Give the extent of all Plasmodium falciparum-infected red blood cells.
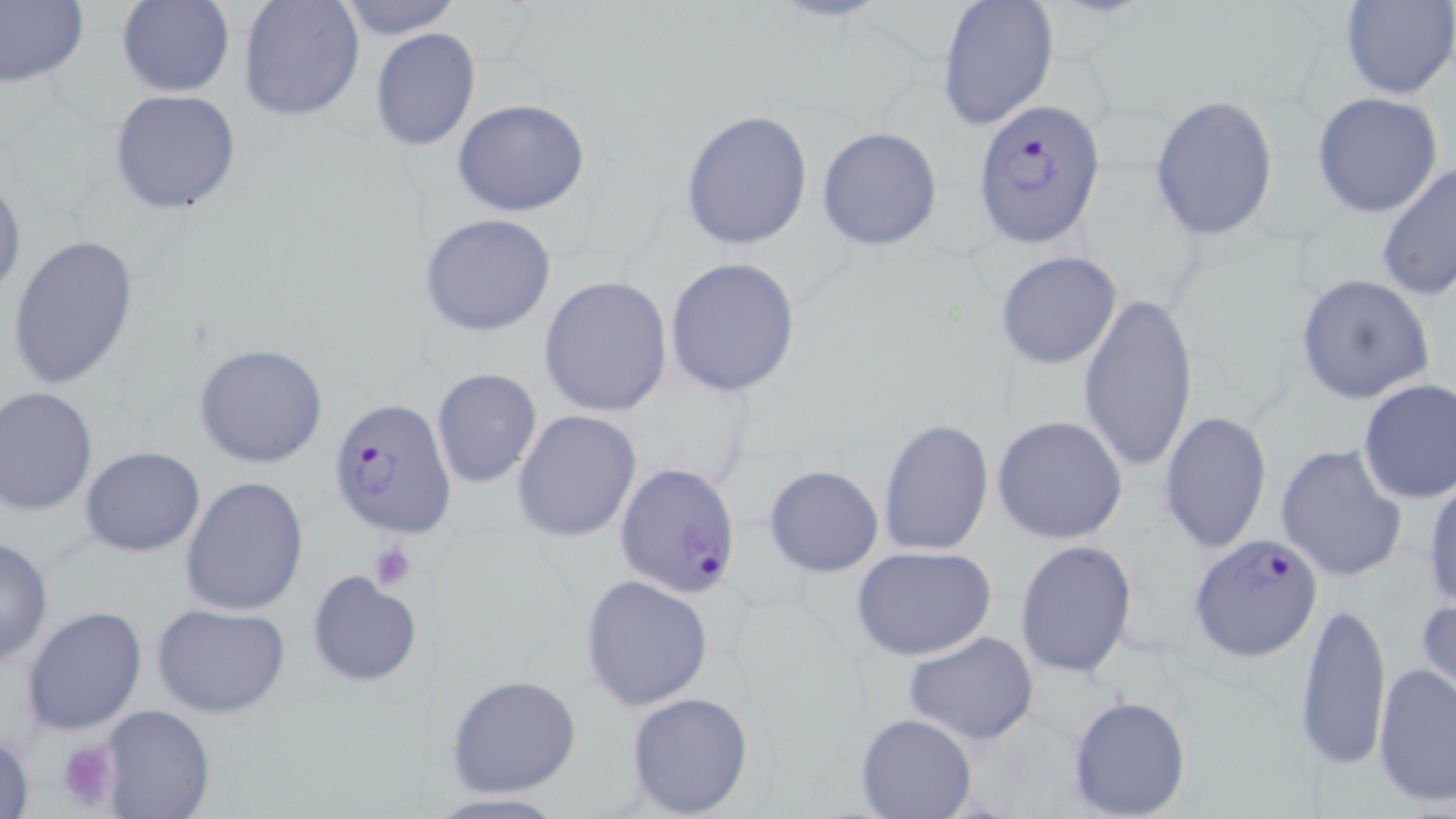

Approximate bounding boxes as (x1, y1, x2, y2) in pixels.
Plasmodium falciparum-infected red blood cells: (973, 98, 1106, 249), (327, 397, 459, 540), (615, 462, 744, 599), (1190, 535, 1324, 662).

Summary:
  - Platelet locations: (367, 544, 417, 590), (58, 739, 123, 813)
  - Uninfected red blood cell locations: (116, 0, 234, 98), (238, 0, 365, 121), (337, 0, 462, 38), (1339, 0, 1456, 101), (0, 1, 88, 87), (937, 1, 1059, 131), (369, 29, 481, 152), (109, 90, 241, 214), (1311, 91, 1444, 218), (1149, 94, 1279, 240), (451, 99, 592, 218), (681, 108, 814, 252), (817, 126, 944, 250), (1378, 163, 1455, 301), (0, 173, 24, 303), (421, 213, 558, 337), (7, 232, 140, 390), (996, 251, 1122, 370), (664, 258, 803, 398), (1295, 273, 1436, 404), (540, 275, 673, 417), (1079, 290, 1198, 476), (195, 344, 329, 467), (431, 368, 542, 490), (1356, 379, 1456, 504), (0, 386, 98, 516), (512, 410, 642, 544), (1159, 410, 1272, 554), (992, 414, 1128, 544), (878, 418, 994, 557), (1277, 444, 1408, 584), (79, 446, 206, 556), (764, 465, 884, 576), (181, 475, 310, 617), (1423, 476, 1456, 612), (0, 535, 54, 667), (1014, 540, 1139, 680), (852, 546, 996, 661), (306, 569, 423, 686), (579, 574, 714, 709), (1416, 594, 1456, 708), (1294, 600, 1392, 771), (152, 604, 291, 717), (20, 605, 149, 735), (902, 631, 1040, 745), (1374, 662, 1455, 810), (445, 674, 582, 798), (624, 691, 754, 818), (1066, 694, 1191, 819), (97, 704, 214, 818), (856, 712, 977, 818), (1, 724, 37, 819), (422, 791, 573, 818)
  - Slide-level diagnosis: Plasmodium falciparum
  - Stain: May-Grünwald-Giemsa
  - Preparation: thin blood smear
  - Image size: 1456×819 pixels
  - Magnification: 1000x
  - Modality: optical microscopy
  - Field of view: single